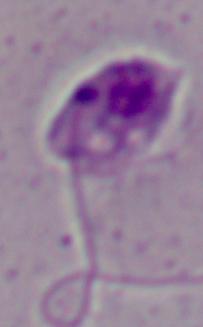

modality = micrograph
magnification = 1000x
identification = Leishmania